State which parasite is depicted.
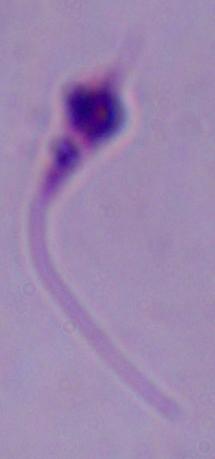
This is Leishmania.

modality: photomicrograph
magnification: 1000x